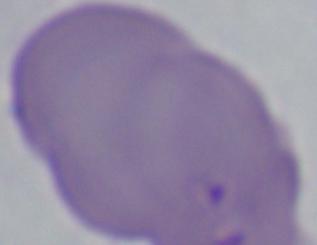

magnification = 1000x
modality = photomicrograph
identification = Babesia